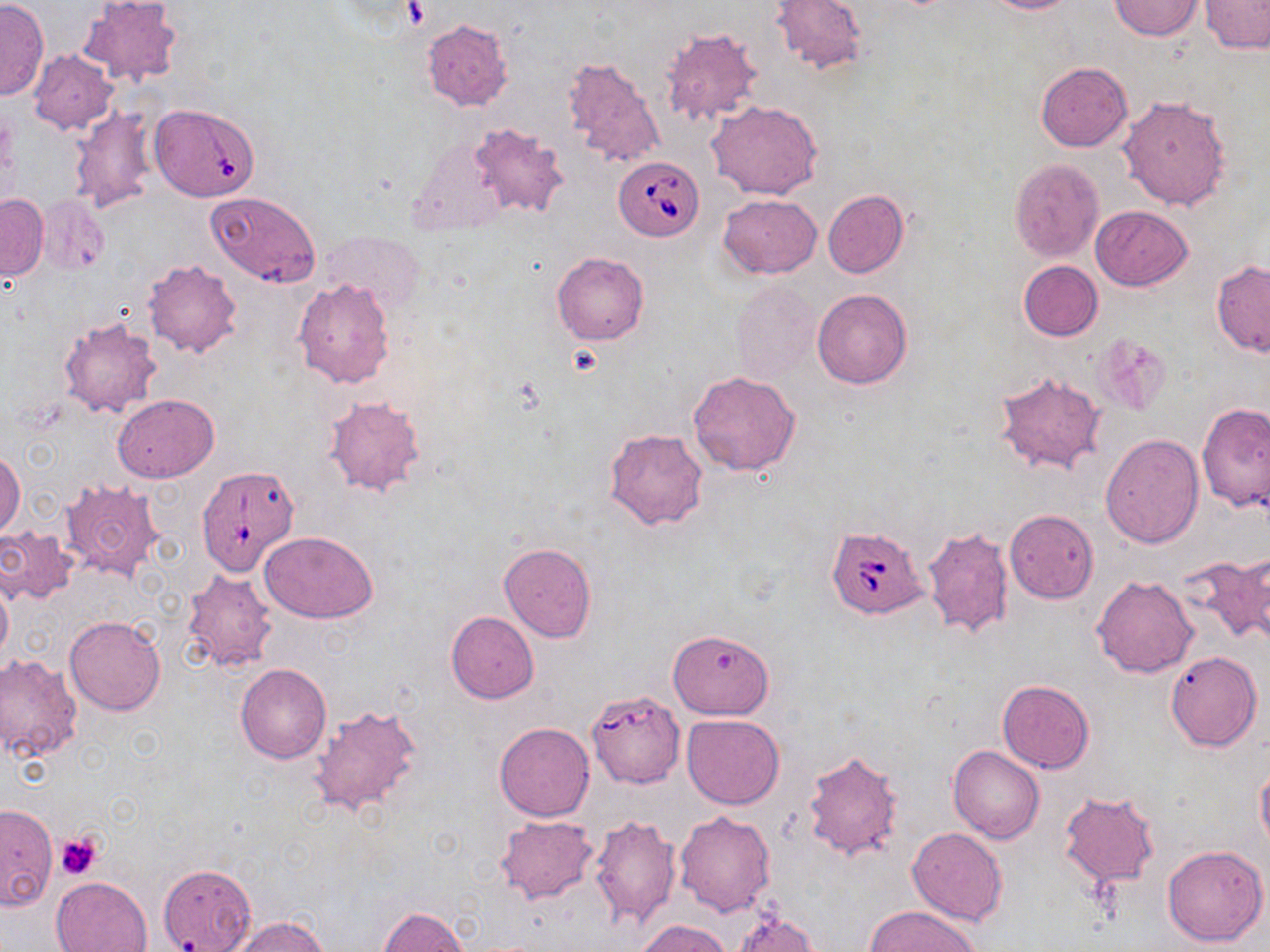
{
  "slide_level_diagnosis": "Babesia divergens",
  "preparation": "thin blood smear",
  "uninfected_red_blood_cell_locations": "approximate bounding boxes as (x1, y1, x2, y2) in pixels: (77, 0, 184, 89), (770, 0, 866, 74), (983, 0, 1083, 14), (1201, 0, 1269, 53), (0, 1, 49, 99), (1109, 1, 1203, 40), (422, 19, 512, 112), (661, 28, 762, 126), (28, 49, 117, 133), (565, 59, 663, 167), (1036, 62, 1132, 152), (1118, 94, 1232, 212), (708, 101, 823, 201), (69, 105, 154, 214), (150, 105, 256, 201), (468, 121, 571, 219), (407, 136, 508, 240), (1009, 158, 1104, 262), (822, 189, 908, 278), (206, 191, 320, 284), (0, 194, 48, 281), (718, 194, 822, 277), (35, 195, 110, 275), (1089, 206, 1193, 290), (324, 231, 424, 317), (552, 251, 648, 344), (1018, 259, 1102, 341), (144, 260, 242, 357), (1212, 260, 1270, 355), (292, 277, 396, 390), (731, 280, 819, 385), (812, 289, 911, 389), (58, 315, 162, 418), (1095, 333, 1171, 413), (994, 369, 1107, 476), (688, 370, 800, 475), (113, 393, 219, 482), (324, 396, 425, 497), (1198, 402, 1270, 511), (606, 428, 709, 531), (1100, 433, 1204, 547), (1, 449, 24, 541), (58, 480, 163, 584), (1005, 510, 1098, 602), (920, 525, 1016, 638), (0, 526, 79, 606), (261, 530, 379, 623), (498, 543, 597, 641), (1228, 551, 1269, 645), (1181, 556, 1266, 648), (181, 570, 278, 674), (0, 573, 13, 667), (1092, 576, 1198, 679), (445, 611, 540, 703), (64, 616, 166, 715), (667, 628, 774, 719), (1166, 651, 1263, 752), (0, 655, 83, 761), (235, 663, 330, 763), (996, 680, 1094, 772), (309, 704, 425, 818), (682, 714, 784, 808), (494, 723, 594, 821), (947, 745, 1045, 845), (803, 749, 903, 861), (1255, 762, 1270, 855), (1059, 791, 1160, 886), (0, 802, 57, 910), (675, 810, 776, 917), (588, 813, 682, 930), (495, 815, 599, 904), (908, 828, 1008, 926), (1161, 843, 1268, 947), (159, 863, 256, 952), (51, 875, 152, 952), (868, 905, 982, 952), (377, 906, 469, 952), (727, 910, 820, 952), (230, 915, 329, 952), (634, 918, 732, 952)",
  "magnification": "1000x",
  "field_of_view": "one of a larger specimen",
  "image_size": "1270×952 pixels",
  "platelet_locations": "approximate bounding boxes as (x1, y1, x2, y2) in pixels: (56, 829, 105, 879)",
  "modality": "light microscopy",
  "stain": "May-Grünwald-Giemsa",
  "babesia_divergens_infected_red_blood_cell_locations": "approximate bounding boxes as (x1, y1, x2, y2) in pixels: (613, 156, 704, 240), (196, 465, 298, 575), (827, 525, 928, 617), (588, 694, 682, 789)"
}